Outline every leukocyte.
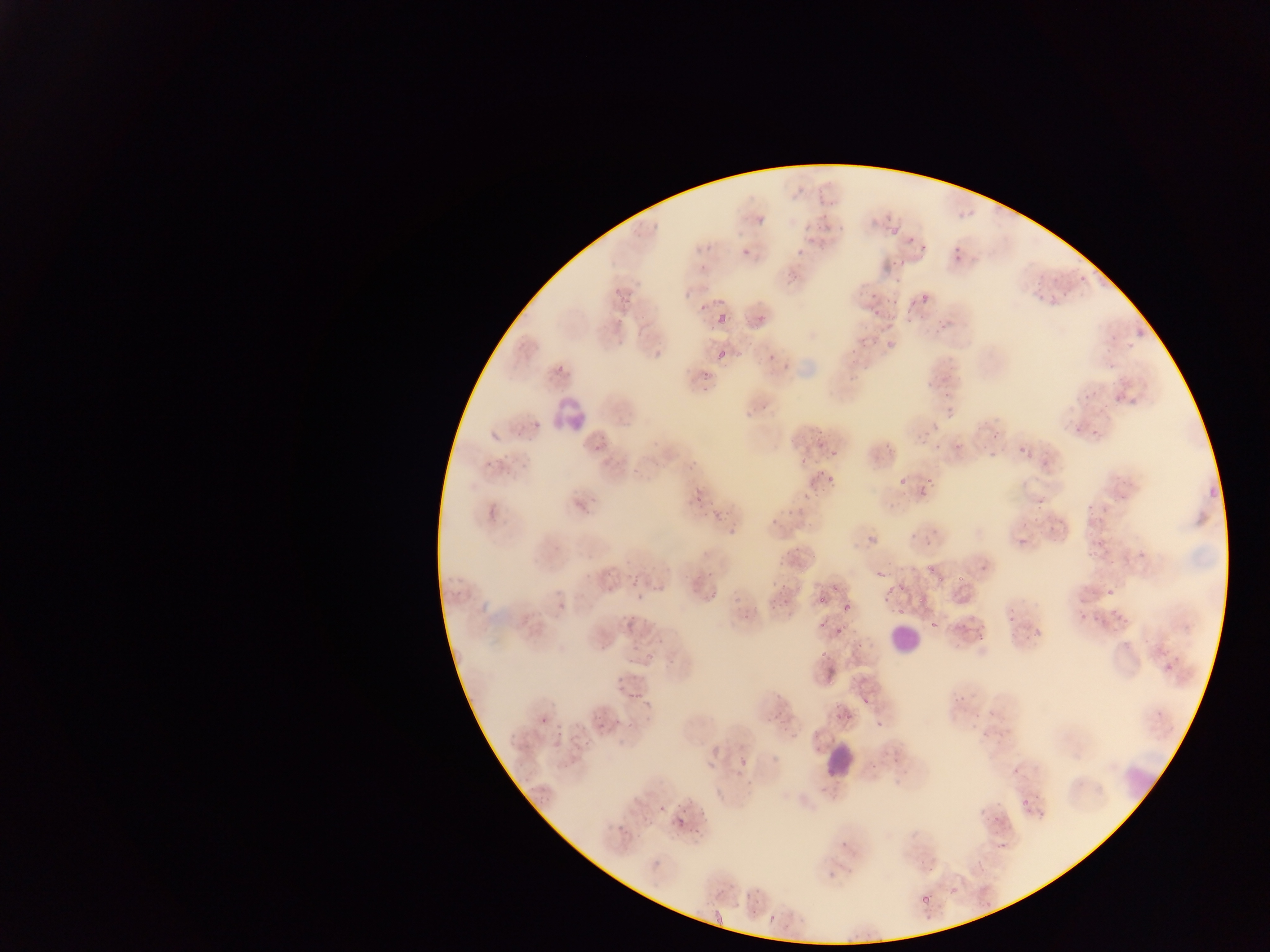

Approximate bounding boxes as left top right bottom in pixels.
Leukocytes: 552 394 593 434; 887 615 931 663; 819 737 863 784.

Malaria parasite locations: 820 210 829 221; 755 211 767 224; 650 219 667 229; 890 221 901 236; 803 222 813 236; 837 223 846 232; 820 227 831 235; 903 233 917 242; 916 238 930 254; 741 243 756 254; 691 245 699 254; 949 246 968 267; 795 247 806 255; 890 255 909 274; 787 266 803 280; 1033 269 1048 281; 893 273 903 282; 1079 274 1093 285; 633 278 643 289; 614 285 623 297; 867 288 878 301; 1035 288 1045 300; 1058 289 1069 298; 916 290 929 306; 682 293 691 299; 888 293 896 305; 619 295 631 306; 1050 295 1058 303; 713 296 728 304; 699 304 706 312; 871 309 879 316; 754 311 767 322; 880 311 897 331; 716 314 728 326; 928 320 945 339; 616 337 624 348; 884 339 893 350; 716 350 729 363; 767 352 776 363; 1107 358 1117 372; 557 362 565 376; 701 372 711 383; 844 373 854 381; 924 374 935 386; 702 384 709 392; 939 389 951 411; 1110 391 1125 405; 1083 392 1094 400; 757 403 771 411; 532 417 541 428; 1076 424 1085 431; 916 428 930 443; 1091 430 1101 438; 989 431 1001 439; 953 436 967 451; 930 441 942 452; 590 443 602 454; 1018 443 1029 455; 883 444 894 454; 986 445 1004 459; 830 446 837 460; 686 458 697 474; 629 467 640 477; 816 469 824 480; 926 473 936 483; 827 477 833 486; 899 477 908 487; 691 483 701 494; 813 484 822 496; 916 486 930 498; 804 489 814 505; 693 497 700 505; 1034 499 1045 513; 711 507 718 520; 721 508 729 519; 1029 512 1042 520; 768 515 781 526; 1047 519 1061 532; 726 528 735 539; 867 535 876 549; 1018 535 1031 545; 923 538 934 546; 1082 544 1100 558; 775 555 786 564; 922 558 936 573; 603 567 613 575; 706 568 715 578; 876 570 887 582; 630 573 640 585; 886 573 899 594; 955 573 965 584; 899 577 910 588; 934 578 943 585; 773 581 785 591; 607 583 615 594; 654 583 662 594; 1106 586 1116 594; 635 592 645 603; 709 592 717 600; 818 592 828 602; 916 594 924 604; 780 596 793 608; 769 597 781 612; 555 599 569 615; 1112 602 1121 612; 839 603 850 612; 1006 606 1016 620; 894 608 901 616; 1115 608 1133 624; 1077 609 1088 622; 820 610 830 635; 1092 611 1103 628; 740 612 752 625; 624 615 635 631; 1031 625 1045 633; 973 633 989 643; 652 636 668 644; 852 636 866 648; 630 641 641 652; 644 644 659 663; 820 647 830 662; 619 683 627 689; 630 685 648 697; 862 692 875 703; 952 694 964 703; 641 698 648 708; 774 703 789 723; 834 706 850 721; 989 707 998 715; 974 711 983 723; 611 713 621 726; 539 715 547 722; 598 715 610 728; 780 715 796 732; 553 723 563 735; 982 725 996 739; 507 732 519 747; 791 732 799 743; 738 754 749 764; 563 759 575 770; 705 761 712 769; 736 768 747 778; 688 793 696 807; 1033 795 1044 800; 1019 798 1030 806; 701 802 710 813; 977 804 989 815; 1025 804 1036 819; 660 806 667 814; 994 808 1008 819; 673 813 685 825; 614 819 624 832; 693 822 699 832; 837 834 852 847; 998 837 1013 850; 826 869 839 877; 950 883 963 898; 755 891 769 907; 920 892 937 905; 769 911 780 922 | approximate x y pixel centers of objects too small to bound: 709 246; 619 320; 657 440; 819 444; 803 459; 836 588; 630 723; 1016 773. Thin blood film. One field of view. Sample from Ghana. Mobile-phone photograph taken through the microscope. Image is 1270×952 pixels.